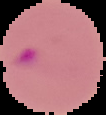
Summary:
  - Image type: cell region segmented out of the field of view; surrounding area masked to black
  - Preparation: thin blood smear
  - Malaria status: parasitized
  - Image size: 106×115 pixels